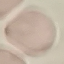

result = no malaria parasites seen
image type = cell patch, automatically extracted from a larger field of view and resized to 64 × 64 pixels
preparation = thin smear
capture = smartphone through the microscope eyepiece
stain = Giemsa